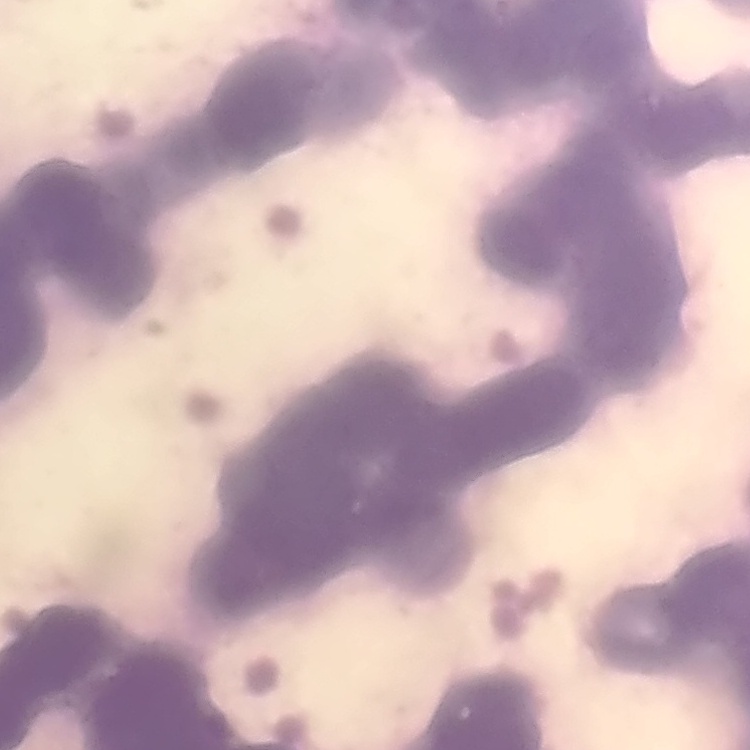
Summary:
  - Red blood cell morphology: rouleaux formation
  - Image type: one tile cut from a larger photomicrograph
  - Stain: Field's or Giemsa
  - Preparation: thin blood smear